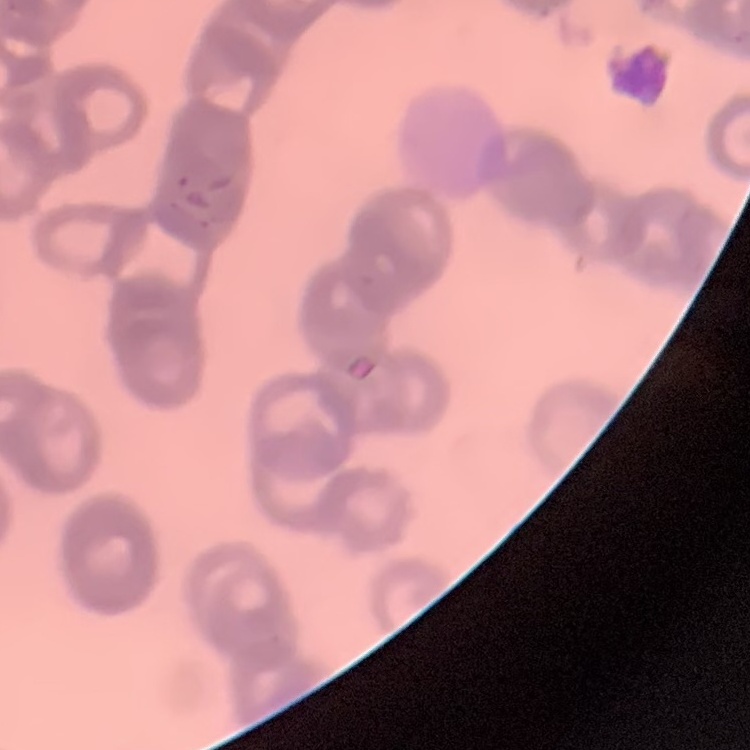 The erythrocytes show rouleaux formation. One tile cut from a larger photomicrograph. Thin blood film. Field's or Giemsa stain.